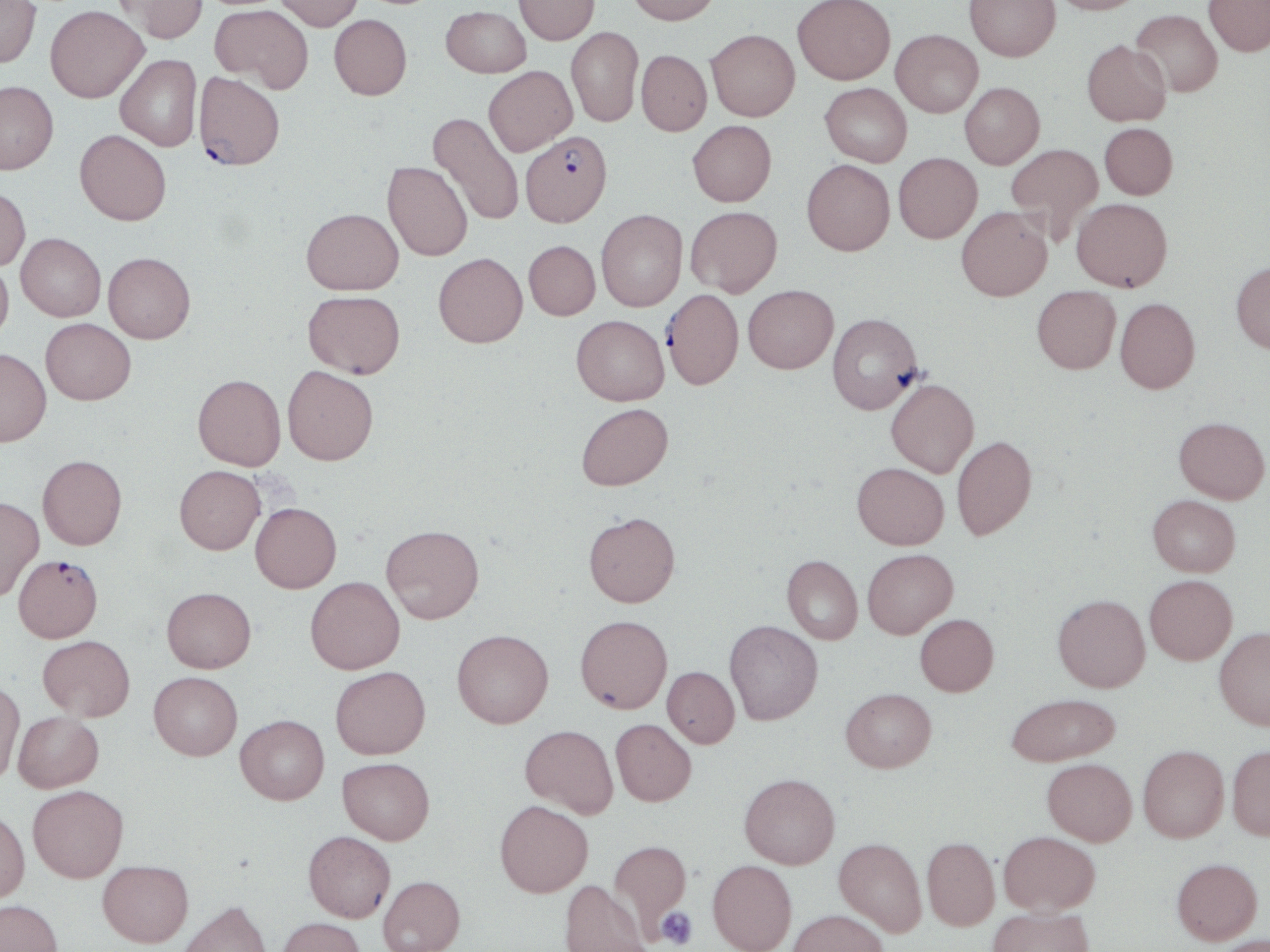

slide-level diagnosis = Plasmodium falciparum
image size = 1270×952 pixels
preparation = thin blood smear
magnification = 1000x
modality = light microscopy
stain = May-Grünwald-Giemsa
Plasmodium falciparum-infected red blood cell locations = approximate bounding boxes as (x1,y1)-(x2,y2) corner pairs in pixels: (194,72)-(285,170), (520,130)-(612,226), (661,289)-(743,389), (13,554)-(103,643)
field of view = one of a larger specimen
uninfected red blood cell locations = approximate bounding boxes as (x1,y1)-(x2,y2) corner pairs in pixels: (113,0)-(208,43), (275,0)-(363,30), (514,0)-(599,45), (626,0)-(720,25), (793,0)-(895,84), (965,0)-(1060,60), (1049,0)-(1146,15), (1204,0)-(1270,56), (0,1)-(41,67), (211,4)-(313,92), (45,5)-(148,102), (441,5)-(531,77), (1131,9)-(1223,97), (329,14)-(412,99), (566,27)-(643,127), (706,29)-(800,121), (891,29)-(983,117), (1082,40)-(1171,126), (636,49)-(712,135), (115,54)-(202,151), (484,66)-(577,155), (0,80)-(59,174), (820,82)-(912,166), (960,82)-(1044,168), (427,111)-(524,226), (687,120)-(776,206), (1099,122)-(1178,199), (75,129)-(171,225), (1006,143)-(1103,242), (893,152)-(982,243), (802,159)-(895,255), (382,161)-(473,261), (0,185)-(30,270), (1071,198)-(1172,291), (686,206)-(782,297), (956,206)-(1052,301), (302,207)-(403,294), (596,209)-(687,311), (16,233)-(106,321), (524,240)-(600,320), (103,252)-(196,343), (434,253)-(528,347), (0,260)-(13,343), (1231,261)-(1270,353), (743,285)-(838,373), (1032,285)-(1120,373), (303,290)-(405,378), (1115,297)-(1200,393), (828,312)-(924,413), (571,315)-(669,405), (41,318)-(136,404), (0,348)-(51,446), (282,366)-(378,465), (193,373)-(286,470), (886,379)-(979,477), (576,403)-(673,490), (1174,417)-(1269,503), (951,435)-(1037,541), (37,454)-(127,549), (852,462)-(949,549), (174,465)-(265,554), (1148,494)-(1240,576), (0,496)-(44,601), (250,502)-(341,593), (583,511)-(680,606), (381,524)-(484,623), (862,548)-(958,638), (782,555)-(863,643), (1145,575)-(1237,664), (305,576)-(405,674), (162,586)-(256,672), (1052,594)-(1150,692), (914,613)-(999,696), (575,615)-(673,713), (724,620)-(822,725), (1214,626)-(1270,729), (452,629)-(553,728), (38,635)-(135,721), (330,666)-(430,759), (662,666)-(740,748), (149,671)-(243,760), (0,679)-(24,785), (840,688)-(936,773), (1005,693)-(1121,766), (13,712)-(104,792), (236,715)-(329,804), (611,719)-(696,806), (520,724)-(618,818), (1227,744)-(1270,839), (1138,745)-(1229,842), (338,757)-(435,844), (1042,758)-(1137,846), (739,773)-(840,868), (28,785)-(128,882), (495,800)-(593,897), (0,810)-(30,902), (304,831)-(395,922), (999,831)-(1100,915), (834,837)-(926,936), (922,837)-(1000,930), (608,840)-(692,937), (1171,858)-(1263,945), (98,860)-(193,946), (707,860)-(797,952), (378,875)-(465,952), (560,880)-(650,952), (0,899)-(63,952), (177,900)-(273,952), (987,906)-(1093,952), (787,909)-(887,952), (277,917)-(365,952), (1212,935)-(1270,952)
platelet locations = approximate bounding boxes as (x1,y1)-(x2,y2) corner pairs in pixels: (656,906)-(697,950)